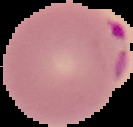
image type = segmented cell region on a black background
preparation = thin blood smear
malaria status = parasitized
image size = 133×127 pixels